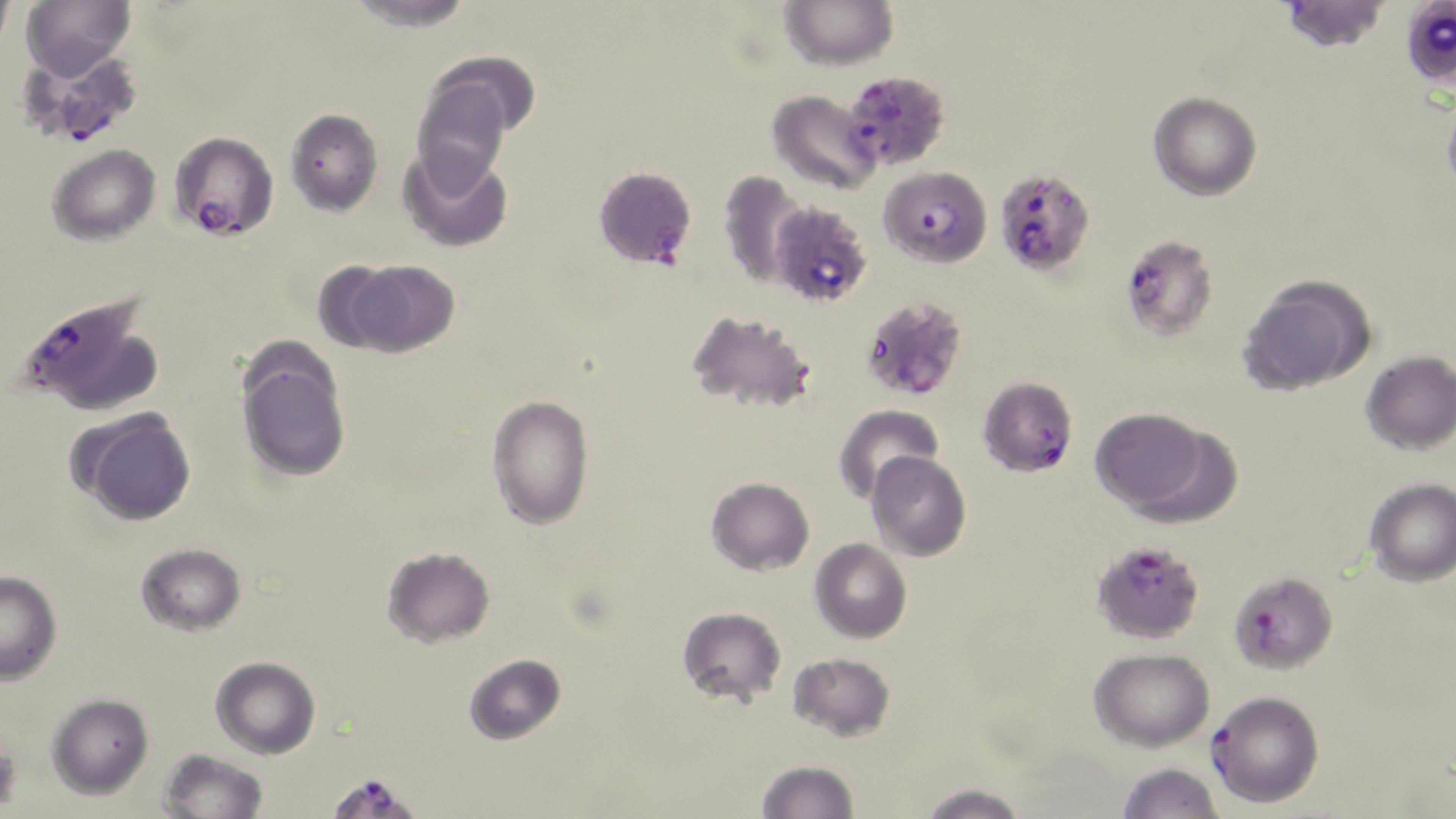

Summary:
  - Coordinate format: approximate bounding boxes as named x1/y1/x2/y2 corners in pixels
  - Uninfected red blood cell locations: (x1=0, y1=0, x2=15, y2=56), (x1=21, y1=0, x2=136, y2=78), (x1=346, y1=0, x2=476, y2=31), (x1=780, y1=0, x2=898, y2=71), (x1=1280, y1=0, x2=1389, y2=52), (x1=1410, y1=6, x2=1453, y2=92), (x1=423, y1=52, x2=540, y2=145), (x1=412, y1=71, x2=515, y2=188), (x1=768, y1=89, x2=881, y2=195), (x1=1148, y1=91, x2=1262, y2=201), (x1=1442, y1=93, x2=1456, y2=200), (x1=285, y1=107, x2=383, y2=216), (x1=47, y1=144, x2=160, y2=245), (x1=398, y1=144, x2=513, y2=253), (x1=718, y1=171, x2=808, y2=290), (x1=345, y1=259, x2=460, y2=357), (x1=311, y1=260, x2=403, y2=354), (x1=1238, y1=276, x2=1373, y2=395), (x1=686, y1=310, x2=815, y2=415), (x1=1360, y1=351, x2=1456, y2=455), (x1=237, y1=352, x2=351, y2=482), (x1=486, y1=393, x2=594, y2=530), (x1=835, y1=403, x2=943, y2=503), (x1=1089, y1=408, x2=1210, y2=514), (x1=73, y1=410, x2=197, y2=526), (x1=1129, y1=423, x2=1246, y2=528), (x1=866, y1=451, x2=971, y2=561), (x1=706, y1=477, x2=814, y2=575), (x1=1364, y1=478, x2=1456, y2=587), (x1=809, y1=538, x2=912, y2=643), (x1=136, y1=543, x2=246, y2=636), (x1=382, y1=546, x2=495, y2=647), (x1=0, y1=570, x2=62, y2=684), (x1=677, y1=606, x2=786, y2=706), (x1=1090, y1=648, x2=1215, y2=751), (x1=788, y1=652, x2=895, y2=741), (x1=464, y1=653, x2=566, y2=744), (x1=211, y1=656, x2=320, y2=759), (x1=47, y1=692, x2=153, y2=799), (x1=0, y1=726, x2=23, y2=818), (x1=158, y1=749, x2=268, y2=819), (x1=757, y1=760, x2=859, y2=819), (x1=1115, y1=762, x2=1224, y2=819), (x1=917, y1=783, x2=1029, y2=819)
  - Plasmodium falciparum-infected red blood cell locations: (x1=16, y1=44, x2=143, y2=148), (x1=840, y1=69, x2=951, y2=173), (x1=168, y1=130, x2=279, y2=241), (x1=882, y1=171, x2=992, y2=269), (x1=598, y1=173, x2=692, y2=274), (x1=1000, y1=176, x2=1095, y2=274), (x1=778, y1=203, x2=871, y2=317), (x1=1120, y1=234, x2=1219, y2=342), (x1=13, y1=291, x2=155, y2=412), (x1=871, y1=306, x2=969, y2=403), (x1=983, y1=385, x2=1078, y2=483), (x1=1095, y1=544, x2=1199, y2=647), (x1=1229, y1=571, x2=1338, y2=674), (x1=1209, y1=690, x2=1324, y2=808), (x1=325, y1=771, x2=423, y2=818)
  - Slide-level diagnosis: Plasmodium falciparum
  - Image size: 1456×819 pixels
  - Stain: May-Grünwald-Giemsa
  - Preparation: thin blood film
  - Modality: optical microscopy
  - Field of view: single
  - Magnification: 1000x